Evaluate for malaria.
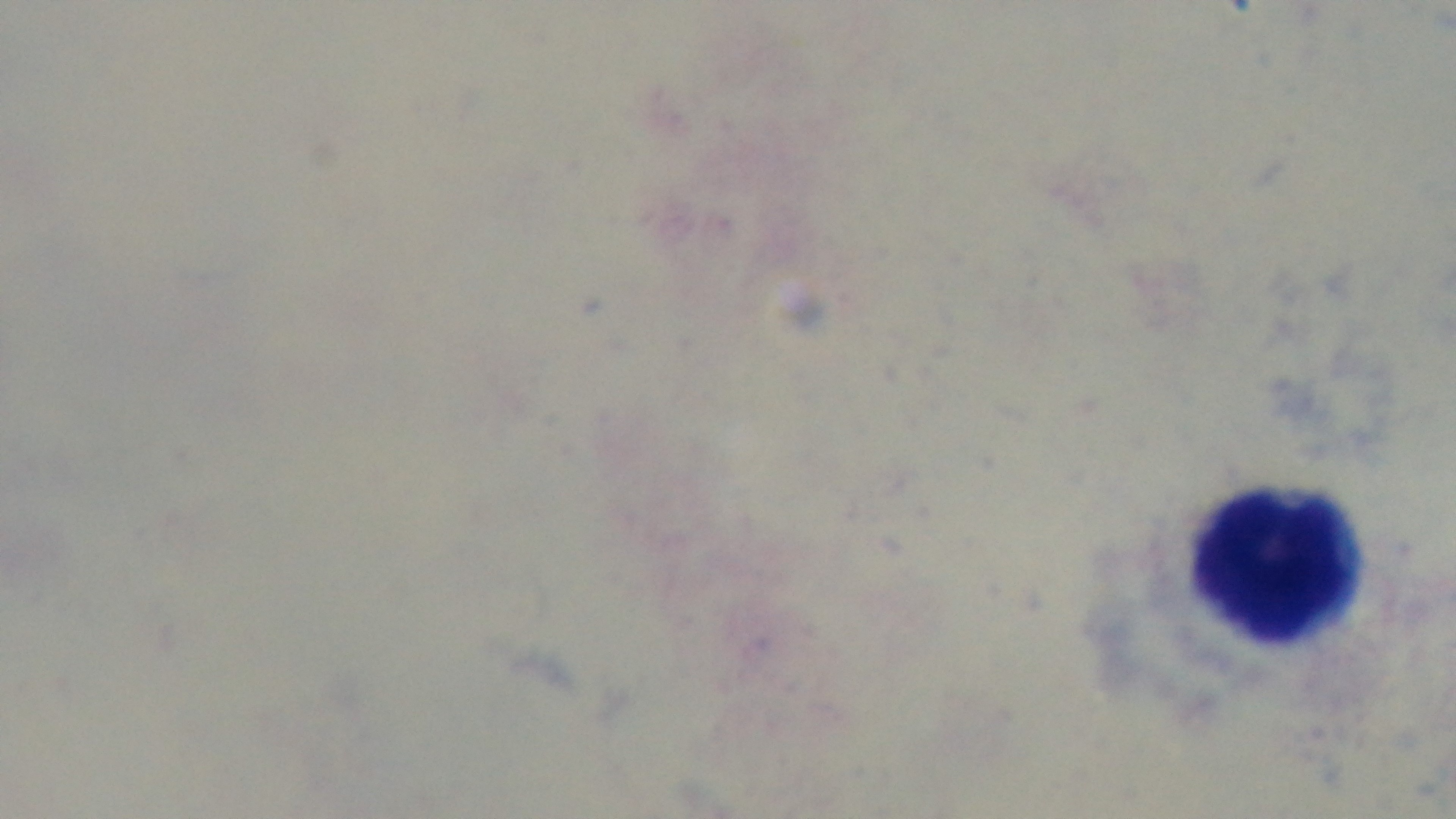
Negative.

Summary:
  - Capture: mounted 4K digital camera
  - Modality: light microscopy
  - Preparation: thick blood film
  - Objective: 100x oil immersion
  - Stain: Giemsa
  - Field of view: single